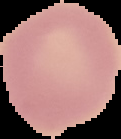
{
  "image_size": "121×139 pixels",
  "preparation": "thin blood smear",
  "malaria_status": "uninfected",
  "image_type": "cell region segmented out of the field of view; surrounding area masked to black"
}